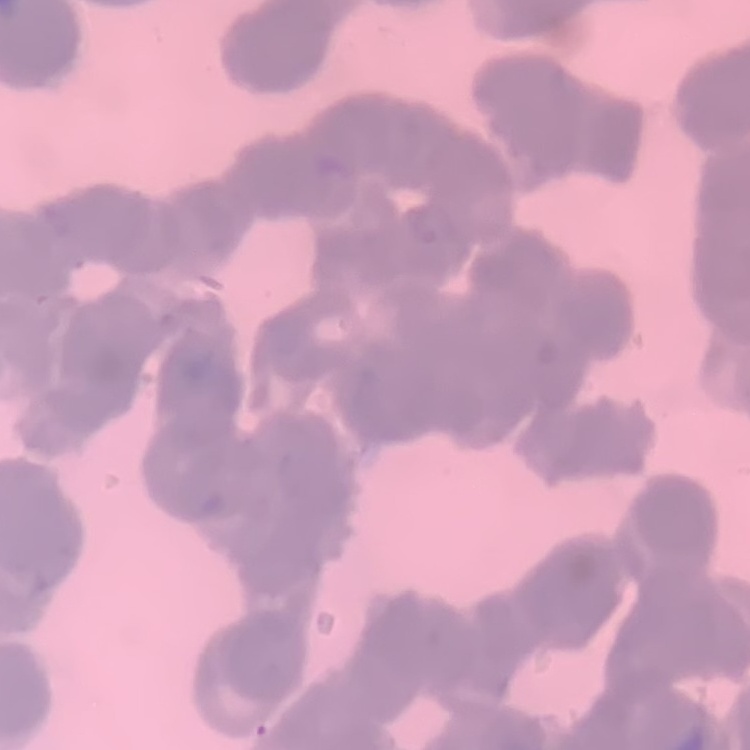

Summary:
  - Erythrocyte morphology: rouleaux formation
  - Preparation: thin blood smear
  - Stain: Field's or Giemsa
  - Image type: one tile cut from a larger photomicrograph